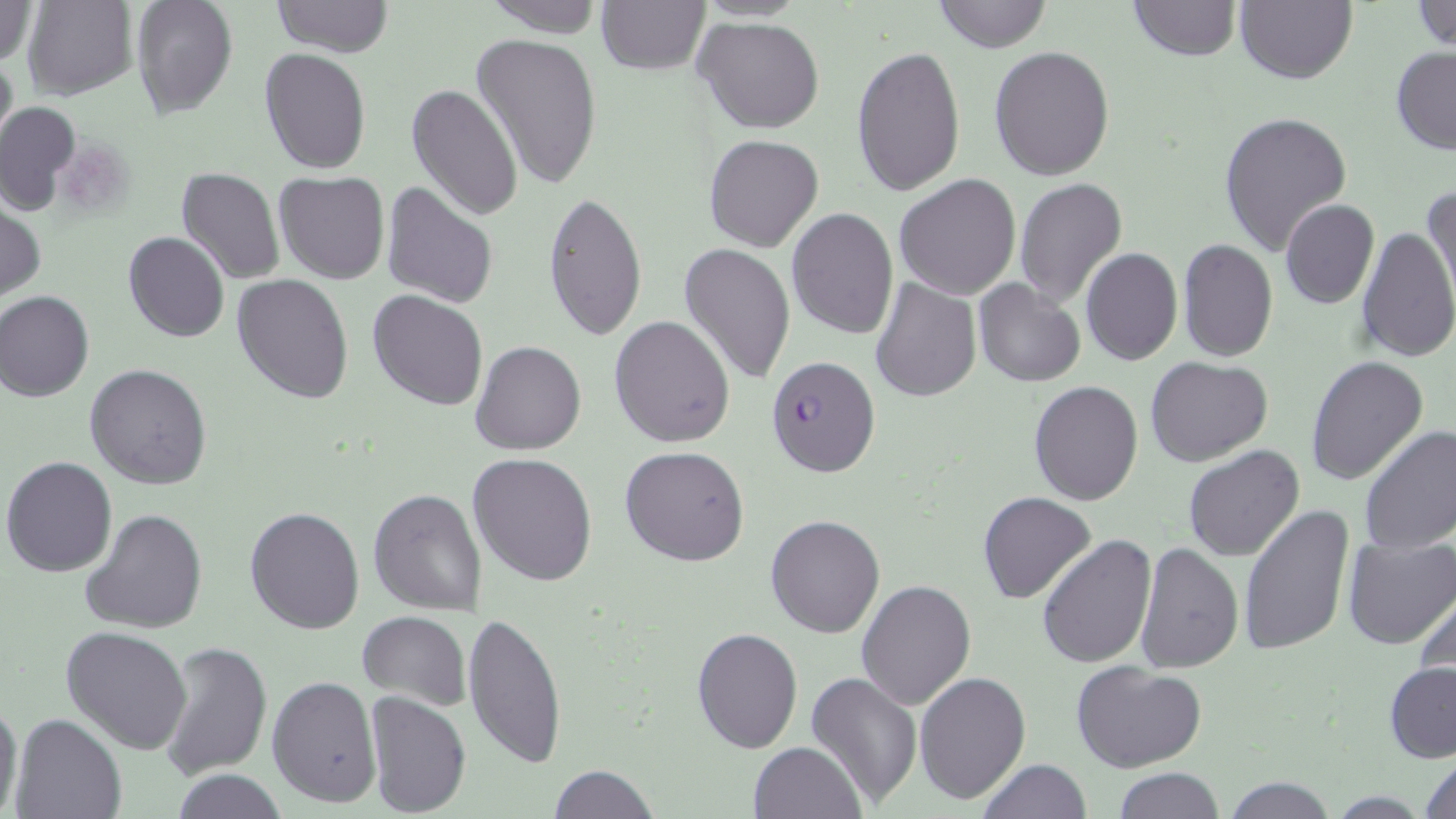
Summary:
  - Coordinate format: approximate bounding boxes as (x1,y1)-(x2,y2) corner pairs in pixels
  - Plasmodium falciparum-infected red blood cell locations: (767,356)-(881,479)
  - Uninfected red blood cell locations: (1,0)-(38,64), (21,0)-(137,99), (128,0)-(239,120), (271,0)-(393,57), (479,0)-(605,36), (932,0)-(1053,53), (1126,0)-(1240,61), (1409,0)-(1456,53), (595,1)-(710,74), (1234,2)-(1357,86), (694,17)-(824,134), (471,33)-(604,190), (850,44)-(966,198), (988,45)-(1115,181), (259,46)-(372,175), (0,47)-(17,157), (1390,47)-(1456,156), (407,81)-(523,221), (0,100)-(80,215), (1218,111)-(1352,257), (704,133)-(824,253), (176,168)-(285,284), (275,171)-(390,285), (894,174)-(1021,299), (1013,178)-(1127,308), (1424,182)-(1455,303), (381,184)-(498,309), (540,191)-(647,341), (1280,198)-(1380,310), (0,202)-(44,300), (787,207)-(897,338), (1355,225)-(1456,365), (124,232)-(231,343), (1177,238)-(1278,363), (678,241)-(796,386), (1081,247)-(1183,365), (231,273)-(355,403), (871,278)-(982,402), (973,279)-(1085,386), (368,289)-(489,411), (0,290)-(95,401), (609,315)-(735,448), (469,340)-(587,456), (1305,355)-(1430,488), (1146,357)-(1273,467), (85,363)-(213,489), (1029,380)-(1143,505), (1359,426)-(1456,556), (620,446)-(750,566), (1184,446)-(1305,563), (467,453)-(598,587), (1,456)-(118,578), (369,487)-(488,614), (977,492)-(1097,605), (245,505)-(366,633), (80,507)-(209,635), (1239,507)-(1355,657), (766,514)-(886,637), (1037,533)-(1156,668), (1342,534)-(1456,649), (1134,541)-(1244,673), (856,579)-(976,710), (1414,585)-(1456,707), (463,610)-(567,770), (357,613)-(471,709), (62,626)-(192,754), (691,627)-(803,754), (159,639)-(271,781), (1072,660)-(1207,771), (1385,661)-(1456,763), (807,671)-(923,810), (915,671)-(1031,805), (267,675)-(381,808), (363,690)-(472,818), (0,698)-(23,818), (9,714)-(126,819), (747,741)-(867,819), (1419,752)-(1456,818), (975,759)-(1091,819), (547,764)-(658,819), (1113,768)-(1225,818), (171,771)-(288,818), (1223,777)-(1339,818)
  - Slide-level diagnosis: Plasmodium falciparum
  - Image size: 1456×819 pixels
  - Stain: May-Grünwald-Giemsa
  - Preparation: thin blood smear
  - Modality: light microscopy
  - Magnification: 1000x
  - Field of view: one of a larger specimen